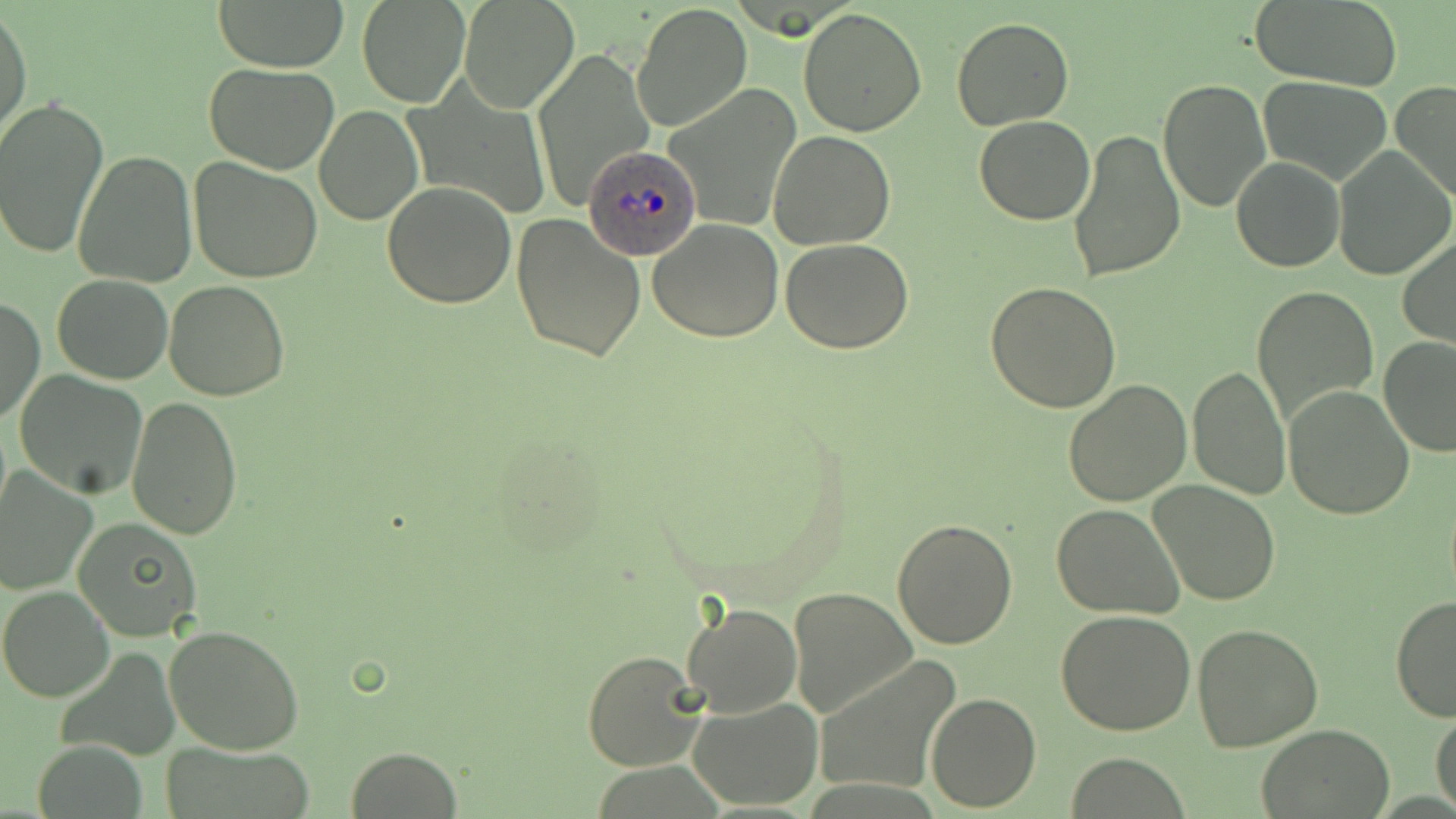
{
  "plasmodium_ovale_infected_red_blood_cell_locations": "approximate bounding boxes as [x1, y1, x2, y2] in pixels: [583, 143, 700, 262]",
  "slide_level_diagnosis": "Plasmodium ovale",
  "image_size": "1456×819 pixels",
  "uninfected_red_blood_cell_locations": "approximate bounding boxes as [x1, y1, x2, y2] in pixels: [210, 0, 349, 72], [356, 0, 471, 108], [459, 1, 578, 114], [1249, 1, 1403, 88], [631, 2, 753, 133], [0, 6, 33, 145], [798, 8, 929, 137], [951, 18, 1074, 130], [531, 48, 654, 207], [203, 62, 339, 173], [1259, 76, 1394, 186], [1159, 77, 1270, 211], [1391, 81, 1456, 205], [665, 85, 803, 233], [0, 95, 108, 264], [313, 105, 423, 225], [974, 115, 1095, 226], [1066, 127, 1186, 284], [768, 128, 896, 249], [1333, 146, 1454, 282], [73, 150, 197, 288], [188, 156, 324, 284], [1231, 157, 1344, 272], [383, 180, 516, 308], [511, 214, 645, 362], [647, 218, 784, 343], [1397, 234, 1456, 349], [779, 237, 915, 353], [51, 274, 175, 384], [164, 281, 291, 402], [984, 282, 1121, 412], [1252, 284, 1380, 429], [1, 298, 45, 425], [1377, 335, 1456, 457], [1189, 362, 1292, 502], [14, 370, 149, 498], [1061, 379, 1191, 505], [1284, 384, 1415, 520], [126, 396, 243, 540], [0, 471, 97, 593], [1149, 481, 1281, 605], [1050, 503, 1185, 619], [73, 518, 202, 642], [893, 518, 1017, 648], [0, 585, 115, 703], [789, 586, 917, 722], [1390, 594, 1456, 724], [680, 602, 802, 718], [1056, 609, 1198, 737], [1193, 623, 1324, 752], [164, 624, 306, 754], [582, 650, 707, 771], [814, 656, 960, 796], [926, 691, 1041, 811], [688, 696, 822, 808], [1431, 706, 1456, 818], [1255, 725, 1394, 817], [34, 740, 147, 819], [162, 742, 318, 819], [345, 746, 463, 819], [1067, 753, 1190, 817]",
  "magnification": "1000x",
  "stain": "May-Grünwald-Giemsa",
  "modality": "light microscopy",
  "field_of_view": "one of a larger specimen",
  "preparation": "thin blood smear"
}